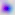

magnification: 400x
identification: Toxoplasma gondii
modality: micrograph